Locate every Plasmodium parasite.
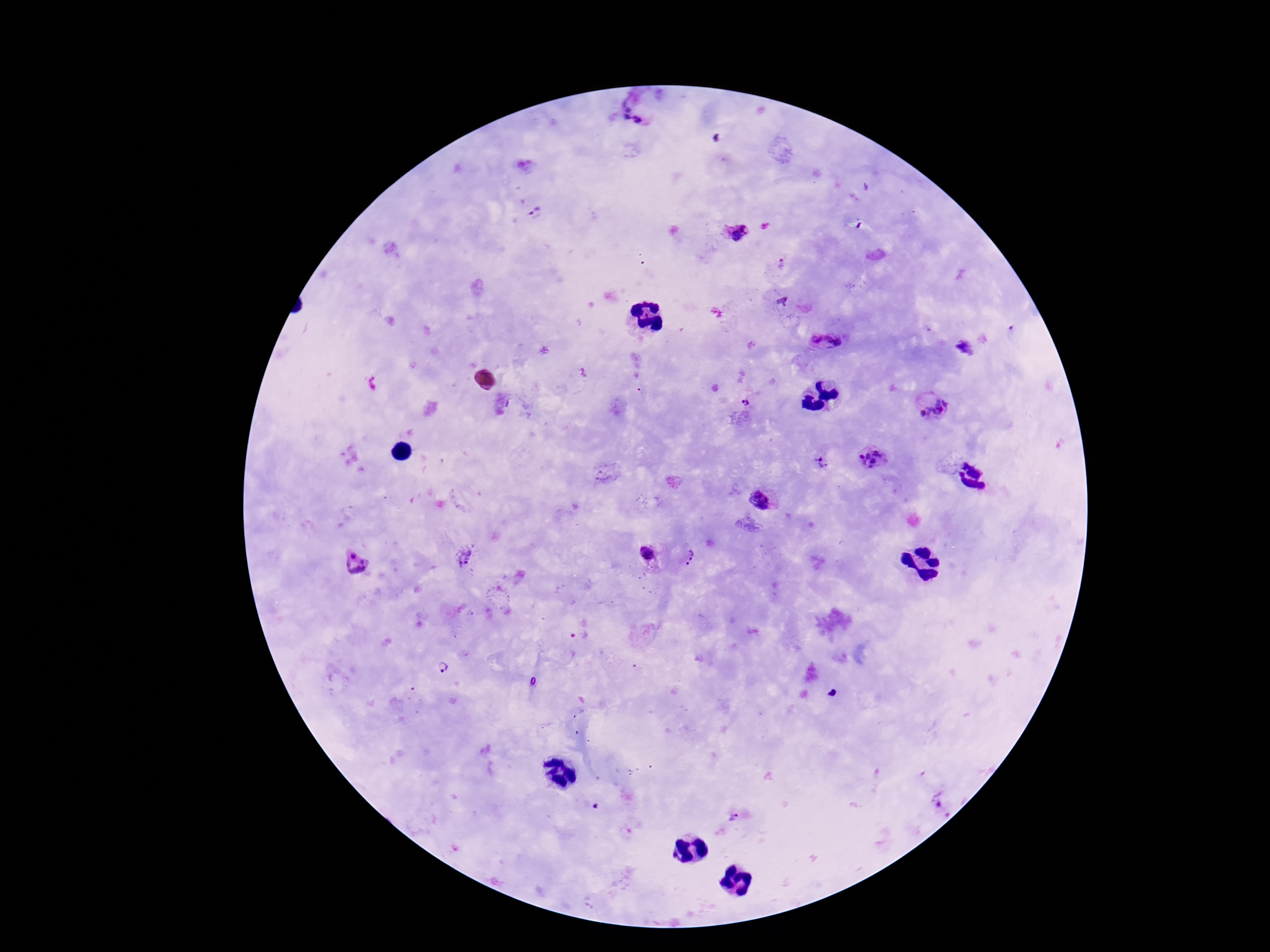

Approximate centers as {x, y} in pixels.
Plasmodium parasites: {629, 108}, {627, 118}, {639, 121}, {537, 215}, {736, 235}, {781, 264}, {815, 338}, {834, 343}, {963, 348}, {746, 402}, {938, 403}, {922, 414}, {871, 458}, {820, 463}, {757, 499}, {353, 554}, {646, 554}, {465, 556}, {691, 558}, {358, 573}, {444, 667}, {735, 819}.

{
  "stain": "Giemsa",
  "magnification": "100x",
  "field_of_view": "single",
  "image_size": "1270×952 pixels",
  "patient_malaria_status": "positive",
  "preparation": "thick blood film",
  "capture": "smartphone camera through the microscope eyepiece"
}